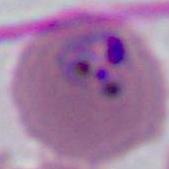
magnification = 400x or 1000x
modality = photomicrograph
identification = Plasmodium